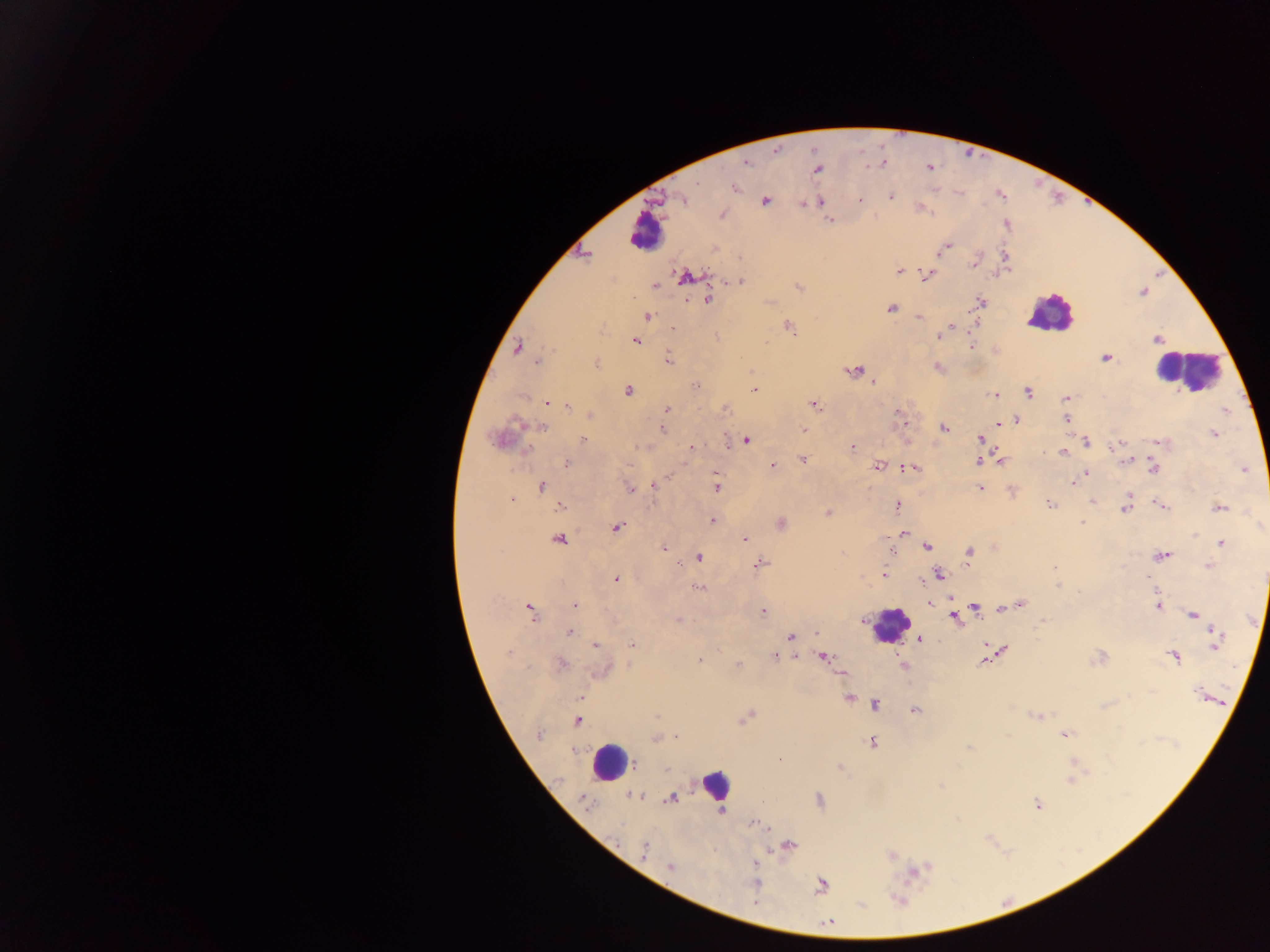 Approximate centers as (x, y) in pixels. Leukocyte locations: (644, 233), (1049, 313), (1186, 370), (890, 625), (609, 762), (715, 785). Plasmodium parasite locations: (883, 163), (746, 164), (817, 169), (735, 188), (891, 197), (681, 199), (765, 200), (859, 200), (820, 202), (802, 204), (722, 214), (830, 221), (944, 249), (584, 256), (1005, 256), (974, 262), (899, 271), (928, 275), (684, 276), (740, 281), (654, 285), (798, 287), (706, 300), (981, 302), (891, 309), (646, 317), (919, 317), (789, 327), (949, 327), (673, 328), (942, 332), (939, 336), (1157, 340), (635, 341), (971, 345), (517, 347), (1106, 358), (668, 359), (537, 363), (596, 364), (938, 368), (855, 371), (873, 383), (696, 386), (755, 390), (628, 391), (1028, 392), (994, 395), (1066, 398), (547, 403), (813, 404), (567, 406), (725, 408), (666, 410), (899, 413), (591, 414), (1065, 418), (1016, 420), (904, 422), (999, 423), (542, 427), (944, 428), (662, 429), (803, 429), (1214, 433), (582, 438), (979, 438), (498, 439), (746, 440), (1086, 441), (1158, 442), (1119, 443), (691, 447), (852, 447), (1062, 452), (802, 460), (1000, 461), (1125, 461), (978, 462), (567, 463), (772, 466), (877, 467), (1154, 467), (910, 468), (1244, 469), (1086, 473), (669, 475), (716, 476), (1073, 483), (542, 486), (654, 486), (716, 487), (631, 489), (980, 489), (511, 500), (1092, 501), (1049, 502), (1161, 506), (560, 507), (898, 507), (1220, 508), (1125, 509), (828, 513), (712, 520), (781, 523), (1082, 523), (616, 528), (903, 533), (558, 539), (745, 539), (1221, 543), (927, 547), (665, 548), (892, 551), (968, 553), (1162, 557), (699, 558), (760, 564), (1209, 566), (1054, 568), (885, 574), (939, 574), (616, 579), (1059, 586), (699, 587), (950, 599), (930, 604), (1020, 604), (575, 605), (1158, 606), (974, 607), (529, 609), (1003, 609), (764, 611), (1194, 615), (953, 617), (677, 619), (1044, 622), (569, 633), (816, 634), (791, 636), (920, 639), (1216, 640), (632, 644), (595, 645), (597, 646), (1003, 649), (508, 652), (774, 656), (797, 657), (1173, 657), (823, 658), (700, 660), (985, 662), (561, 663), (738, 665), (602, 671), (842, 673), (1197, 693), (581, 697), (848, 698), (875, 705), (915, 710), (657, 716), (1036, 716), (745, 718), (576, 722), (538, 735), (1065, 735), (676, 736), (654, 739), (872, 742), (969, 748), (779, 759), (635, 765), (840, 768), (1071, 779), (941, 786), (633, 795), (672, 798), (820, 800), (585, 802), (1037, 804), (721, 811), (753, 824), (789, 846), (644, 850), (892, 855), (757, 862), (669, 867), (756, 882), (822, 885), (756, 902), (828, 922). Collected in Ghana. Single field of view. Image is 1270×952 pixels. Photographed through a microscope with a mobile-phone camera. Thick blood smear.